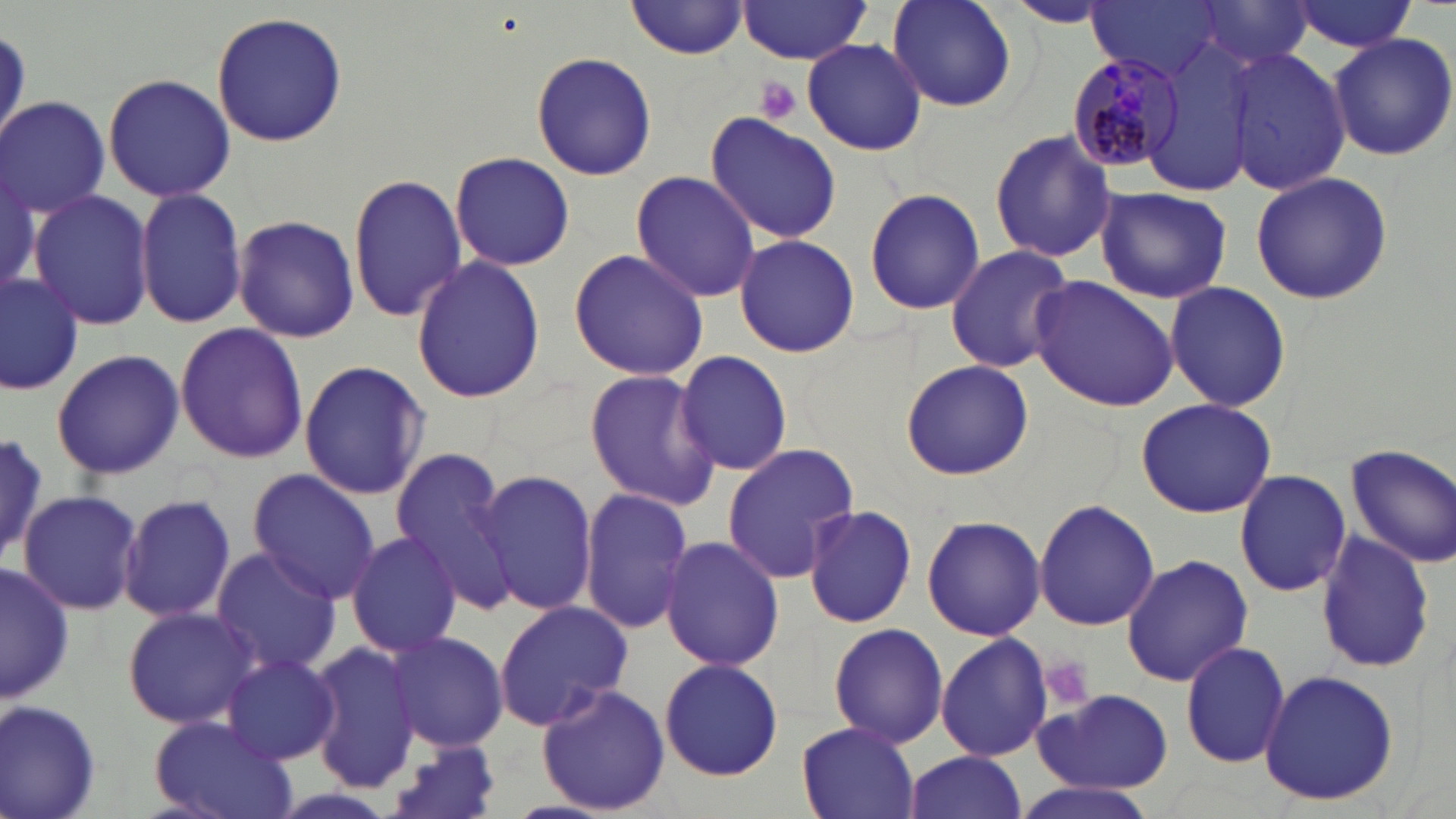 Approximate bounding boxes as [x1, y1, x2, y2] in pixels. Uninfected red blood cell locations: [626, 1, 749, 59], [886, 1, 1019, 114], [1192, 1, 1316, 75], [736, 2, 878, 64], [1287, 2, 1421, 53], [1003, 3, 1121, 29], [1090, 3, 1219, 77], [212, 11, 346, 147], [1327, 31, 1456, 161], [1143, 33, 1265, 192], [801, 38, 926, 156], [1227, 47, 1351, 196], [529, 51, 658, 181], [103, 73, 234, 202], [1, 97, 110, 217], [702, 113, 842, 244], [990, 128, 1117, 263], [450, 151, 575, 272], [0, 157, 40, 302], [629, 170, 763, 303], [1250, 170, 1392, 305], [348, 172, 468, 325], [1095, 186, 1233, 304], [135, 187, 249, 328], [864, 188, 985, 317], [27, 190, 156, 330], [232, 215, 361, 342], [732, 234, 859, 357], [944, 245, 1075, 374], [568, 246, 708, 383], [410, 256, 548, 405], [0, 270, 82, 396], [1028, 275, 1179, 413], [1166, 281, 1291, 412], [175, 321, 307, 464], [50, 347, 185, 479], [673, 349, 794, 475], [298, 359, 431, 502], [900, 359, 1033, 481], [583, 369, 721, 510], [1137, 398, 1277, 519], [0, 433, 50, 567], [720, 443, 859, 582], [1346, 443, 1456, 568], [388, 449, 519, 610], [471, 468, 598, 617], [1235, 469, 1351, 597], [248, 470, 378, 602], [578, 488, 693, 637], [19, 489, 143, 614], [119, 494, 237, 623], [1033, 499, 1160, 631], [803, 503, 918, 629], [923, 515, 1046, 642], [344, 529, 462, 659], [1315, 531, 1436, 672], [658, 534, 784, 671], [209, 546, 341, 677], [1122, 553, 1253, 687], [0, 561, 74, 707], [493, 599, 634, 728], [121, 604, 264, 730], [828, 622, 949, 749], [386, 630, 509, 752], [935, 633, 1054, 762], [306, 639, 422, 793], [1180, 640, 1290, 768], [221, 653, 341, 765], [657, 656, 785, 781], [1259, 668, 1399, 807], [536, 681, 670, 816], [1033, 689, 1174, 793], [0, 699, 103, 819], [148, 713, 300, 819], [796, 722, 921, 819], [381, 737, 507, 819], [902, 752, 1027, 819], [1008, 780, 1163, 819]. Plasmodium malariae-infected red blood cell locations: [1065, 50, 1186, 173]. Platelet locations: [753, 77, 801, 126], [1038, 657, 1094, 711]. Slide-level diagnosis: Plasmodium malariae. Single field of view. 1000x magnification. May-Grünwald-Giemsa-stained preparation. Thin blood film. Image is 1456×819 pixels. Light microscopy.